Give the extent of all Plasmodium falciparum-infected red blood cells.
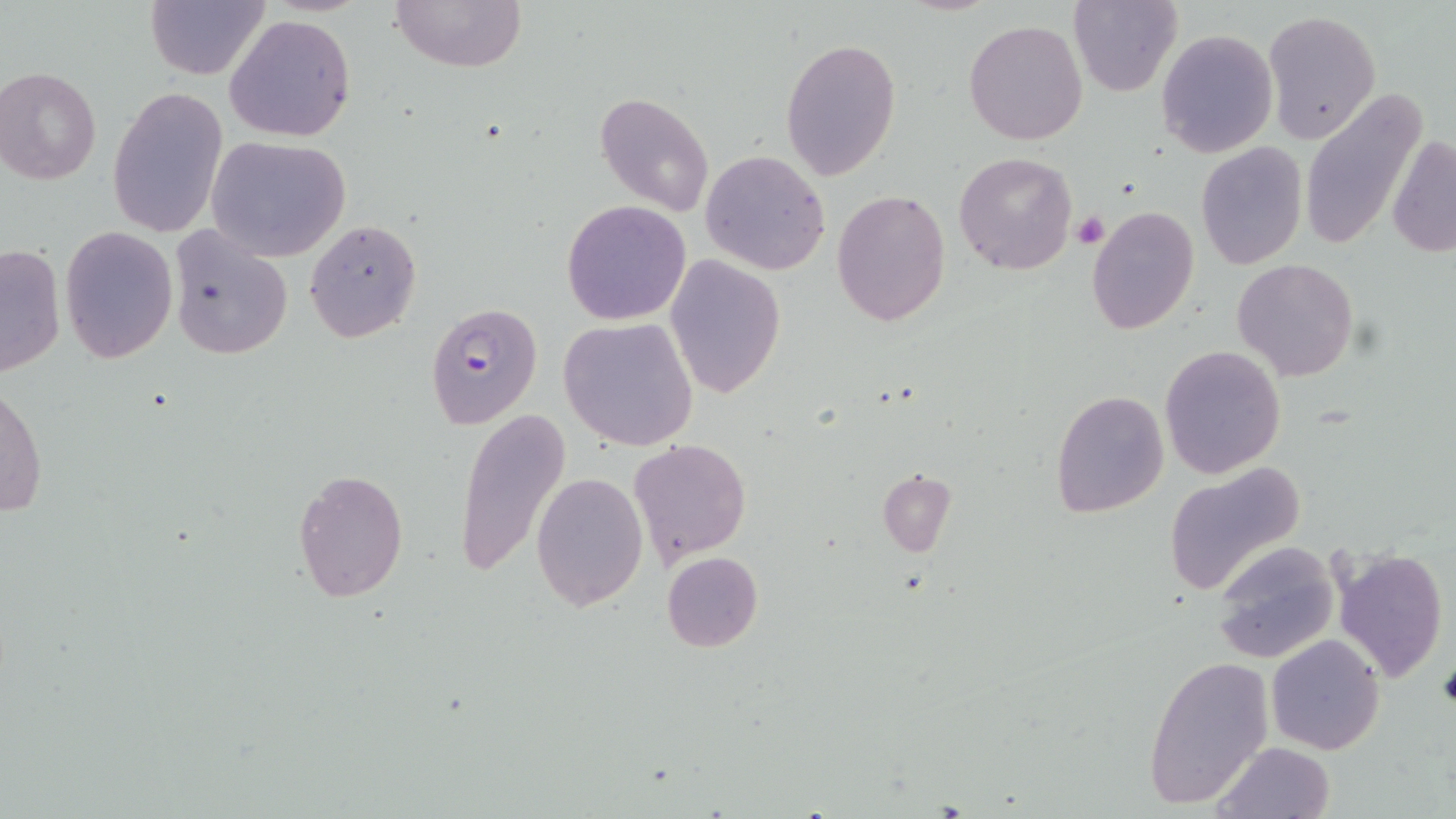
Approximate bounding boxes as (x1, y1, x2, y2) in pixels.
Plasmodium falciparum-infected red blood cells: (424, 302, 543, 430).

Uninfected red blood cell locations: (389, 0, 528, 74), (1069, 0, 1181, 95), (145, 2, 268, 80), (1262, 10, 1381, 143), (223, 14, 356, 142), (962, 19, 1089, 146), (1156, 28, 1278, 157), (783, 37, 901, 183), (1, 67, 101, 184), (108, 86, 229, 239), (596, 91, 716, 218), (1298, 91, 1428, 252), (1388, 133, 1455, 259), (206, 135, 352, 261), (1195, 143, 1307, 268), (700, 150, 831, 275), (953, 151, 1079, 276), (832, 189, 952, 327), (562, 200, 692, 324), (1085, 205, 1199, 334), (304, 218, 423, 343), (60, 225, 177, 364), (167, 225, 293, 361), (0, 242, 66, 380), (663, 255, 785, 399), (1232, 258, 1359, 382), (559, 317, 698, 451), (1159, 344, 1286, 478), (0, 383, 48, 518), (1050, 389, 1170, 519), (451, 408, 570, 580), (628, 437, 752, 567), (1164, 462, 1308, 598), (292, 468, 408, 602), (878, 471, 955, 556), (531, 473, 649, 611), (1211, 541, 1341, 663), (1333, 547, 1449, 685), (661, 551, 764, 653), (1266, 634, 1384, 754), (1144, 654, 1274, 808), (1211, 742, 1335, 819). Platelet locations: (1071, 212, 1108, 249), (1437, 657, 1456, 712). Slide-level diagnosis: Plasmodium falciparum. Thin blood smear. Captured at 1000x magnification. Optical microscopy. Image is 1456×819 pixels. May-Grünwald-Giemsa stain. Single field of view.